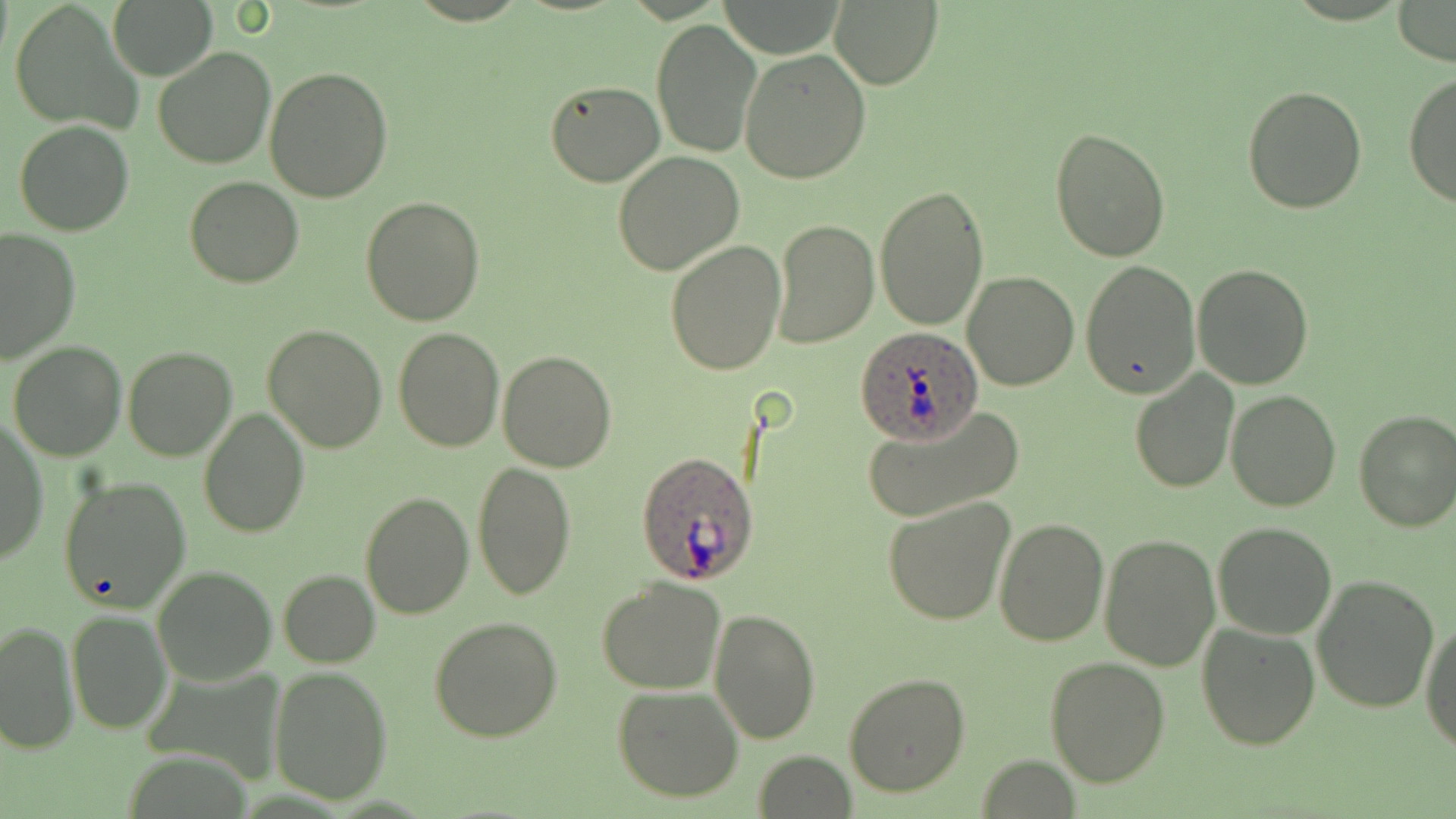
Approximate bounding boxes as (x1,y1)-(x2,y2) corner pairs in pixels. Uninfected red blood cell locations: (107,0)-(218,81), (828,0)-(943,90), (1391,0)-(1455,66), (8,2)-(139,134), (650,18)-(761,159), (738,45)-(872,184), (152,46)-(275,169), (262,66)-(394,202), (1404,72)-(1456,211), (543,79)-(664,186), (1242,84)-(1368,214), (14,120)-(134,236), (1049,126)-(1173,263), (611,152)-(745,276), (185,177)-(304,289), (875,183)-(988,331), (360,197)-(485,325), (770,219)-(878,348), (0,228)-(80,364), (664,239)-(785,376), (1080,258)-(1200,397), (1192,264)-(1313,388), (963,270)-(1080,391), (260,324)-(387,452), (393,325)-(502,450), (7,340)-(127,461), (122,347)-(236,462), (497,350)-(617,472), (1130,370)-(1240,492), (1226,391)-(1342,512), (859,402)-(1025,524), (198,406)-(309,537), (1352,409)-(1456,531), (0,417)-(49,564), (471,459)-(576,600), (60,475)-(192,613), (360,492)-(474,619), (883,496)-(1015,627), (992,516)-(1109,647), (1213,522)-(1338,639), (1098,531)-(1221,671), (151,566)-(276,685), (279,570)-(381,667), (1312,573)-(1439,712), (598,578)-(727,694), (710,605)-(820,744), (67,611)-(170,734), (429,616)-(563,741), (1421,616)-(1455,755), (1,620)-(78,754), (1197,621)-(1322,750), (1045,656)-(1171,787), (268,666)-(393,804), (842,672)-(969,797), (611,686)-(744,802), (754,750)-(857,819). Plasmodium ovale-infected red blood cell locations: (854,327)-(983,441), (636,450)-(761,585). Slide-level diagnosis: Plasmodium ovale. Image is 1456×819 pixels. Captured at 1000x magnification. Optical microscopy. Thin blood film. One field of a larger specimen. May-Grünwald-Giemsa stain.